Report the malaria status of this cell.
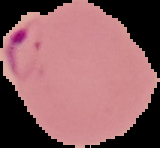
Parasitized.

image_type: cell region segmented out of the field of view; surrounding area masked to black
image_size: 160×148 pixels
preparation: thin blood smear